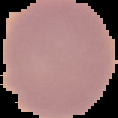

result = no malaria parasites detected
preparation = thin blood smear
image type = segmented cell region on a black background
image size = 118×118 pixels